Give the extent of all Plasmodium falciparum-infected red blood cells.
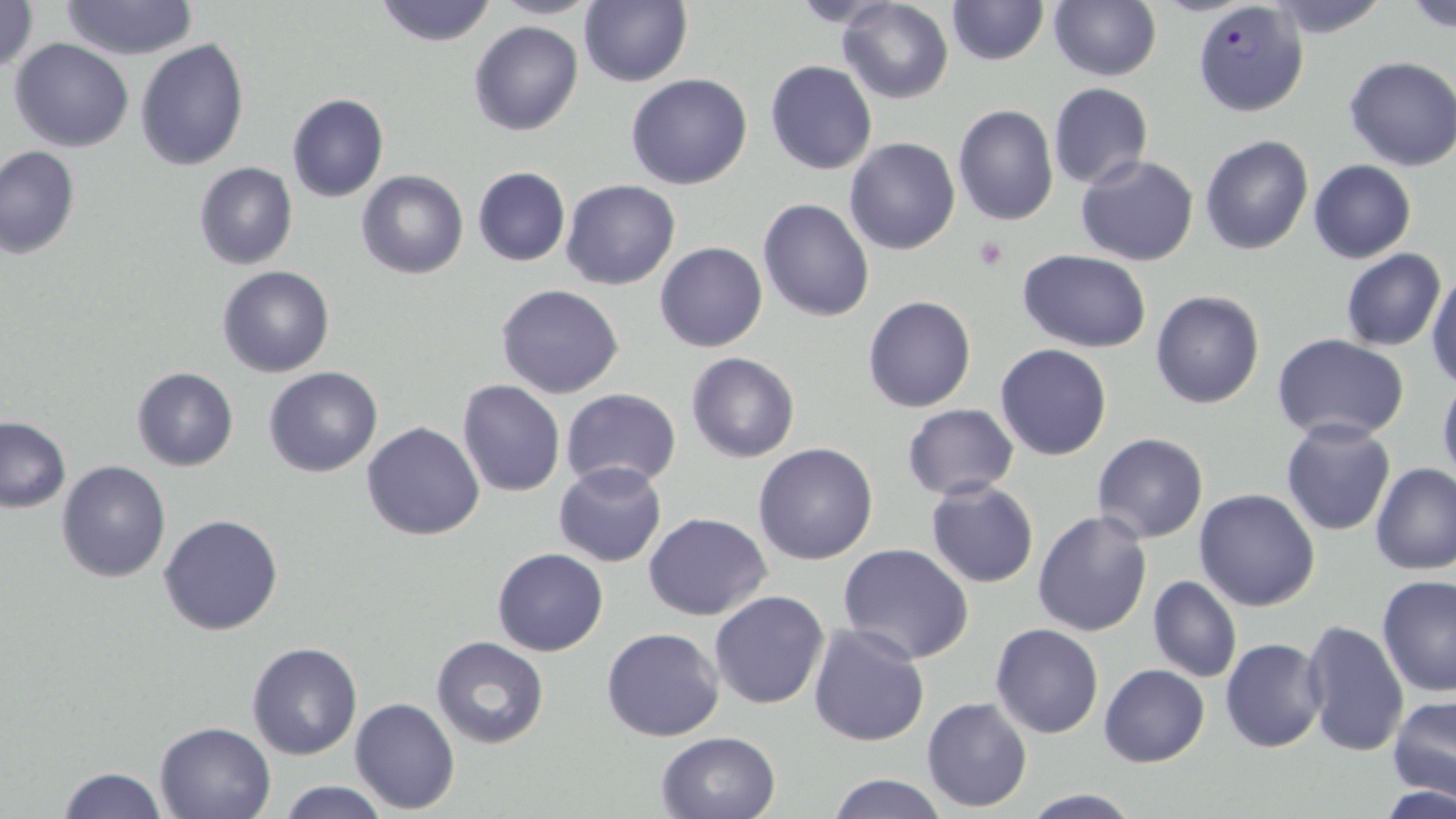
Approximate bounding boxes as named x1/y1/x2/y2 corners in pixels.
Plasmodium falciparum-infected red blood cells: (x1=1192, y1=0, x2=1310, y2=118).

slide-level diagnosis = Plasmodium falciparum
uninfected red blood cell locations = approximate bounding boxes as named x1/y1/x2/y2 corners in pixels: (x1=0, y1=0, x2=38, y2=74), (x1=60, y1=0, x2=199, y2=59), (x1=372, y1=0, x2=498, y2=45), (x1=485, y1=0, x2=602, y2=19), (x1=945, y1=0, x2=1048, y2=66), (x1=1263, y1=0, x2=1391, y2=37), (x1=578, y1=1, x2=692, y2=86), (x1=837, y1=1, x2=955, y2=104), (x1=1404, y1=1, x2=1456, y2=32), (x1=1048, y1=2, x2=1161, y2=81), (x1=468, y1=21, x2=583, y2=136), (x1=8, y1=39, x2=134, y2=152), (x1=134, y1=39, x2=250, y2=171), (x1=1343, y1=56, x2=1456, y2=171), (x1=765, y1=60, x2=878, y2=175), (x1=625, y1=74, x2=753, y2=190), (x1=1048, y1=83, x2=1152, y2=190), (x1=287, y1=93, x2=389, y2=202), (x1=952, y1=103, x2=1059, y2=226), (x1=1200, y1=134, x2=1314, y2=255), (x1=845, y1=138, x2=960, y2=256), (x1=0, y1=145, x2=81, y2=259), (x1=1076, y1=155, x2=1199, y2=267), (x1=785, y1=159, x2=955, y2=296), (x1=1309, y1=159, x2=1416, y2=263), (x1=193, y1=162, x2=298, y2=269), (x1=472, y1=166, x2=571, y2=266), (x1=356, y1=170, x2=469, y2=279), (x1=560, y1=179, x2=681, y2=290), (x1=757, y1=200, x2=874, y2=321), (x1=654, y1=242, x2=768, y2=353), (x1=1340, y1=248, x2=1445, y2=351), (x1=1016, y1=250, x2=1151, y2=350), (x1=216, y1=266, x2=336, y2=379), (x1=1426, y1=272, x2=1456, y2=389), (x1=496, y1=283, x2=625, y2=399), (x1=1150, y1=291, x2=1264, y2=409), (x1=862, y1=295, x2=976, y2=413), (x1=1271, y1=333, x2=1411, y2=442), (x1=994, y1=344, x2=1112, y2=461), (x1=685, y1=353, x2=800, y2=462), (x1=131, y1=367, x2=238, y2=472), (x1=263, y1=367, x2=383, y2=478), (x1=1437, y1=374, x2=1456, y2=489), (x1=457, y1=380, x2=566, y2=497), (x1=561, y1=388, x2=682, y2=489), (x1=901, y1=403, x2=1018, y2=500), (x1=0, y1=417, x2=71, y2=513), (x1=1280, y1=420, x2=1395, y2=536), (x1=361, y1=421, x2=485, y2=541), (x1=1091, y1=433, x2=1211, y2=545), (x1=753, y1=443, x2=878, y2=566), (x1=56, y1=461, x2=170, y2=584), (x1=1370, y1=462, x2=1456, y2=576), (x1=553, y1=463, x2=667, y2=567), (x1=926, y1=479, x2=1040, y2=589), (x1=1194, y1=488, x2=1323, y2=611), (x1=1032, y1=511, x2=1153, y2=637), (x1=644, y1=512, x2=772, y2=621), (x1=158, y1=513, x2=284, y2=636), (x1=837, y1=545, x2=975, y2=665), (x1=492, y1=548, x2=608, y2=657), (x1=1148, y1=575, x2=1241, y2=683), (x1=1376, y1=575, x2=1456, y2=695), (x1=709, y1=591, x2=829, y2=710), (x1=1301, y1=618, x2=1410, y2=757), (x1=991, y1=622, x2=1104, y2=739), (x1=806, y1=623, x2=930, y2=748), (x1=602, y1=627, x2=725, y2=742), (x1=431, y1=637, x2=550, y2=750), (x1=1219, y1=637, x2=1328, y2=753), (x1=246, y1=642, x2=362, y2=760), (x1=1098, y1=664, x2=1210, y2=767), (x1=1387, y1=695, x2=1456, y2=801), (x1=923, y1=696, x2=1033, y2=811), (x1=350, y1=697, x2=459, y2=814), (x1=153, y1=720, x2=278, y2=818), (x1=655, y1=731, x2=780, y2=819), (x1=58, y1=766, x2=167, y2=818), (x1=826, y1=774, x2=949, y2=818), (x1=274, y1=780, x2=394, y2=818), (x1=1385, y1=782, x2=1456, y2=819), (x1=1021, y1=790, x2=1145, y2=818)
stain = May-Grünwald-Giemsa
field of view = one of a larger specimen
platelet locations = approximate bounding boxes as named x1/y1/x2/y2 corners in pixels: (x1=973, y1=236, x2=1010, y2=270)
preparation = thin blood film
image size = 1456×819 pixels
modality = optical microscopy
magnification = 1000x